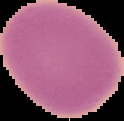
Summary:
  - Preparation: thin blood film
  - Image type: segmented cell region on a black background
  - Result: no malaria parasites seen
  - Image size: 124×121 pixels